Point out each Plasmodium parasite.
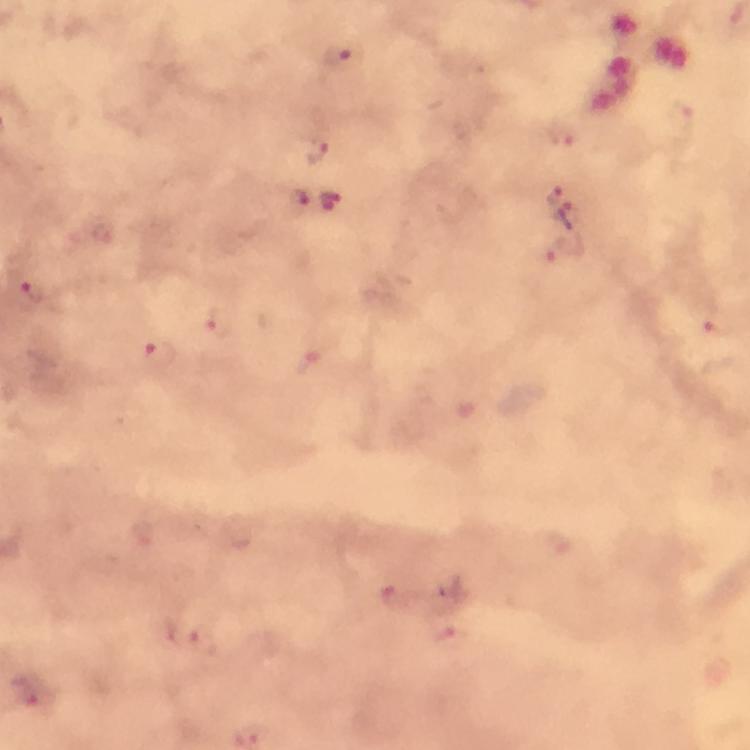

Approximate centers as [x, y] in pixels.
Plasmodium parasites: [338, 56], [684, 119], [562, 135], [317, 149], [553, 195], [330, 201], [297, 204], [574, 215], [559, 251], [34, 293], [221, 324], [713, 326], [159, 354], [202, 640], [35, 692].

Summary:
  - Image size: 750×750 pixels
  - Context: from a malaria diagnostic workup
  - Stain: Giemsa
  - Magnification: 100x
  - Capture: smartphone mounted on the microscope
  - Cropped from: one field of view
  - Preparation: thick blood smear
  - Immersion oil: used